Assess this cell for malaria.
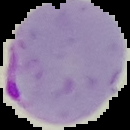
It is parasitized.

Image is 130×130 pixels. From a thin blood smear. The area outside the segmented cell region is set to black.